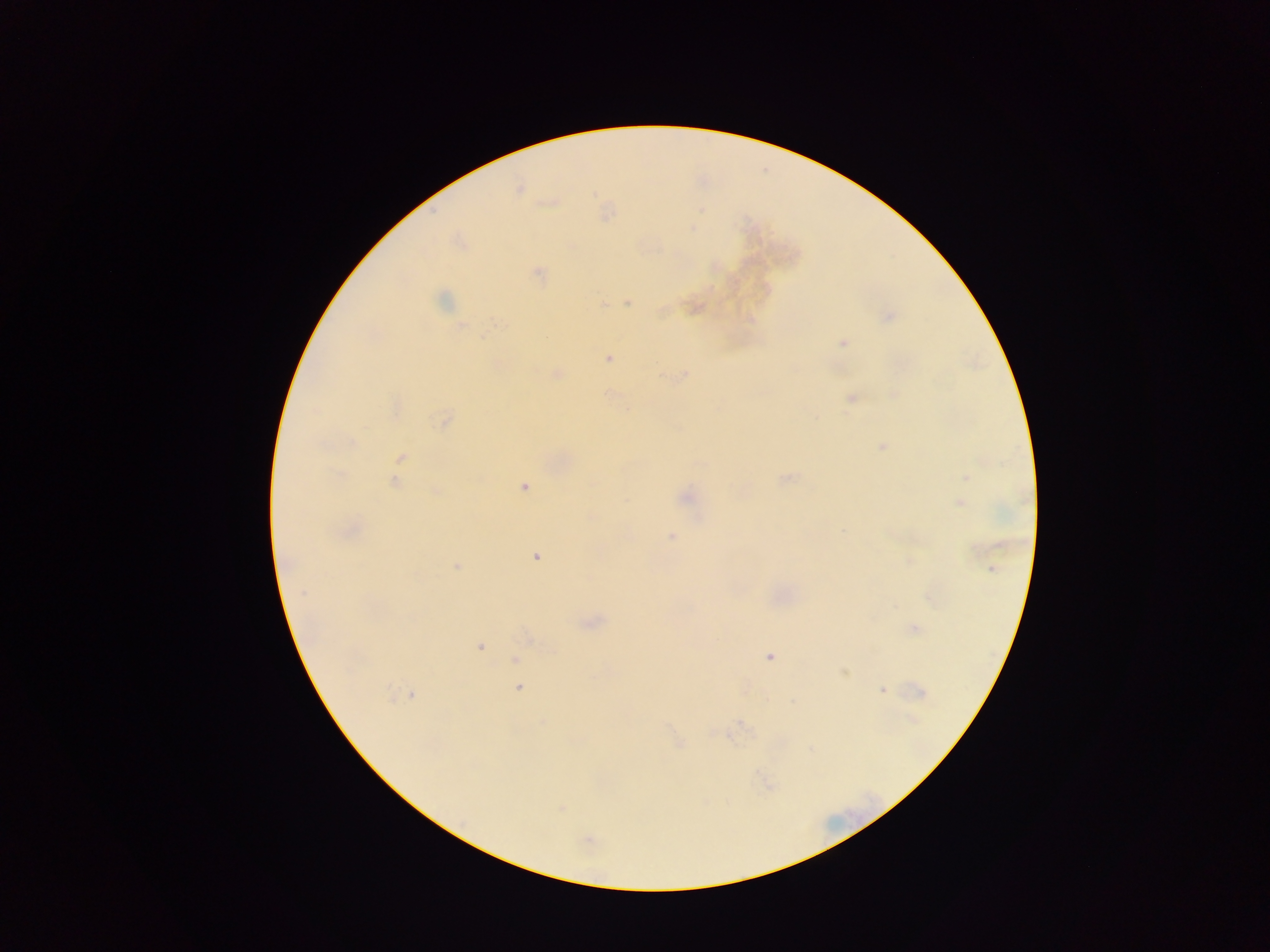

image size = 1270×952 pixels
preparation = thick blood smear
country = Ghana
capture = mobile-phone photograph through a microscope
malaria parasite locations = approximate centers as (x, y) in pixels: (519, 189), (551, 202), (605, 212), (460, 243), (538, 274), (442, 299), (626, 302), (693, 307), (888, 315), (460, 325), (843, 343), (608, 358), (557, 373), (684, 375), (608, 392), (894, 394), (852, 398), (396, 406), (444, 420), (882, 446), (400, 458), (964, 476), (786, 477), (394, 481), (524, 486), (435, 491), (685, 497), (960, 502), (350, 530), (671, 537), (535, 557), (456, 566), (991, 569), (929, 596), (589, 622), (914, 628), (528, 636), (479, 646), (769, 655), (514, 659), (844, 672), (518, 686), (882, 690), (409, 693), (919, 693), (544, 722), (741, 724), (679, 743), (560, 807), (588, 839)
field of view = single